Identify the parasite.
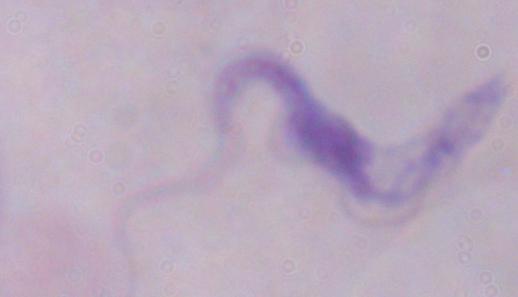
This is a trypanosome.

Summary:
  - Modality: micrograph
  - Magnification: 1000x